Locate every Plasmodium malariae-infected red blood cell.
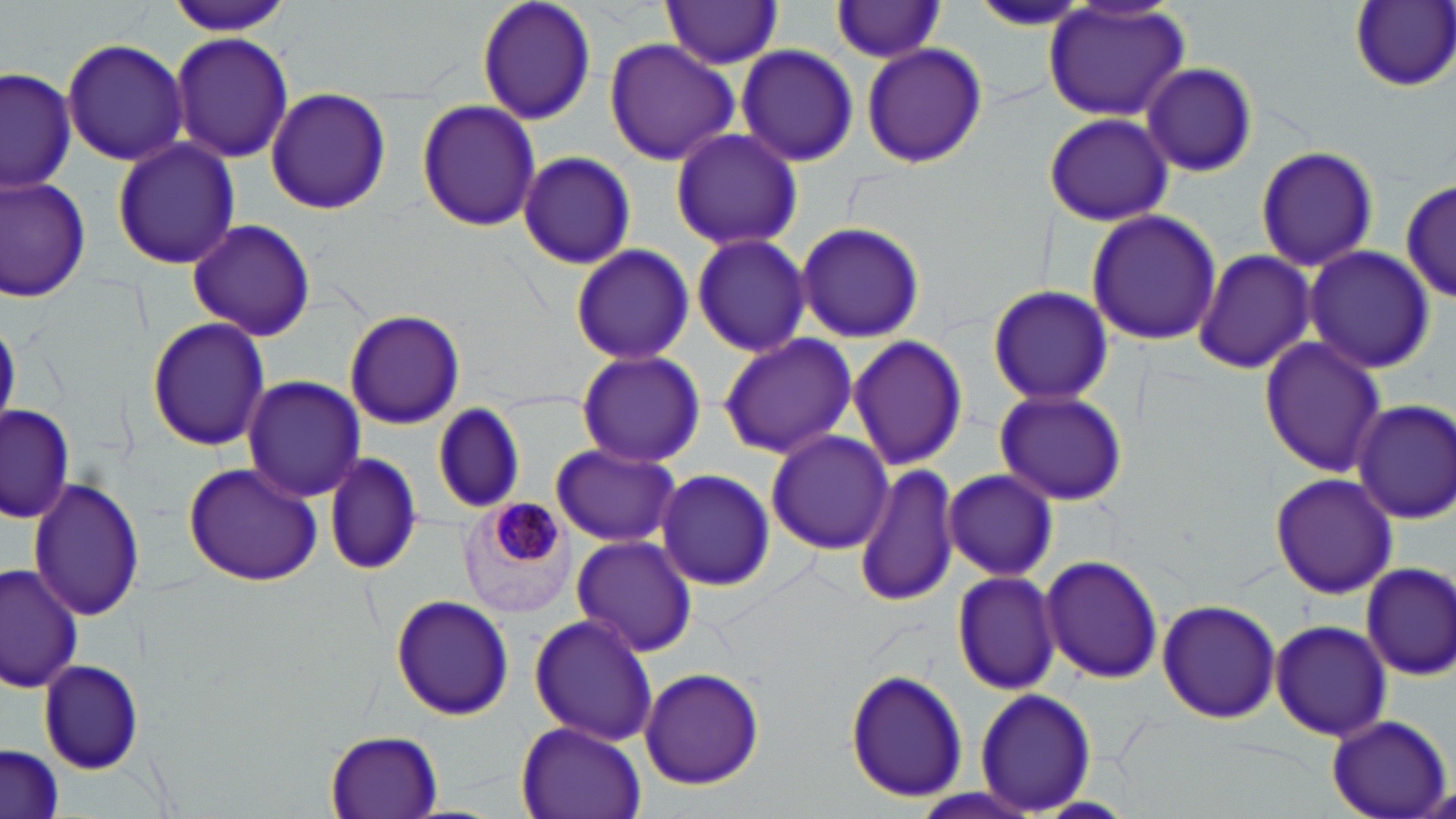

Approximate bounding boxes as [x1, y1, x2, y2] in pixels.
Plasmodium malariae-infected red blood cells: [461, 497, 577, 620].

Summary:
  - Uninfected red blood cell locations: [165, 0, 293, 37], [476, 0, 598, 125], [659, 0, 782, 69], [1350, 0, 1456, 91], [967, 2, 1101, 32], [829, 3, 949, 62], [1042, 3, 1191, 122], [170, 30, 295, 164], [61, 38, 191, 168], [603, 39, 739, 166], [860, 41, 989, 169], [735, 43, 860, 168], [1139, 62, 1259, 175], [1, 66, 77, 194], [264, 87, 391, 215], [416, 100, 541, 232], [1043, 111, 1174, 228], [668, 129, 803, 251], [111, 137, 240, 269], [1255, 145, 1379, 270], [516, 151, 637, 269], [0, 175, 93, 303], [1397, 176, 1453, 307], [1086, 209, 1222, 345], [188, 217, 316, 340], [794, 221, 926, 343], [690, 232, 811, 357], [567, 243, 695, 366], [1302, 245, 1434, 375], [1192, 248, 1318, 377], [987, 286, 1114, 406], [343, 310, 465, 430], [147, 317, 270, 451], [717, 333, 856, 460], [846, 334, 967, 473], [1258, 337, 1388, 476], [576, 351, 704, 466], [241, 376, 367, 501], [994, 388, 1129, 506], [1352, 398, 1456, 525], [2, 401, 75, 525], [431, 402, 523, 515], [764, 430, 894, 556], [550, 442, 681, 548], [321, 450, 423, 577], [853, 459, 961, 608], [181, 460, 325, 587], [943, 468, 1058, 582], [655, 469, 773, 592], [1270, 471, 1397, 600], [27, 477, 145, 621], [571, 536, 699, 657], [1040, 555, 1163, 685], [1359, 563, 1456, 682], [0, 564, 82, 692], [952, 570, 1061, 696], [389, 593, 515, 721], [1156, 599, 1283, 724], [528, 612, 660, 747], [1270, 619, 1392, 742], [39, 658, 144, 774], [637, 668, 765, 791], [844, 668, 967, 804], [975, 687, 1098, 814], [1322, 714, 1453, 819], [515, 722, 646, 819], [325, 731, 442, 816], [2, 745, 66, 819]
  - Slide-level diagnosis: Plasmodium malariae
  - Preparation: thin blood smear
  - Modality: optical microscopy
  - Magnification: 1000x
  - Field of view: one of a larger specimen
  - Image size: 1456×819 pixels
  - Stain: May-Grünwald-Giemsa